Describe the morphology of the red blood cells.
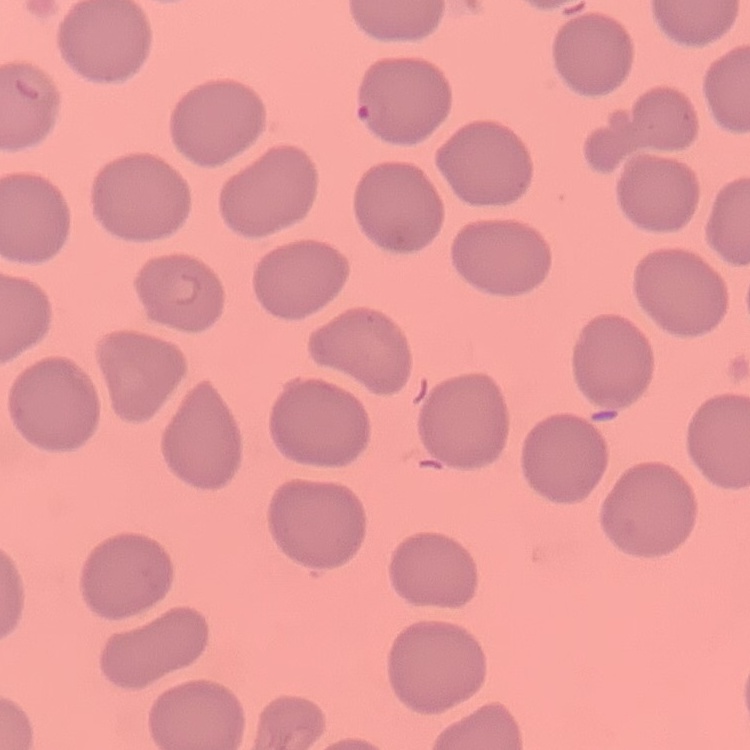
No rouleaux formation.

Summary:
  - Image type: square crop of a larger photomicrograph
  - Preparation: thin peripheral smear
  - Stain: Field's or Giemsa